Give the location of every parasitized red blood cell.
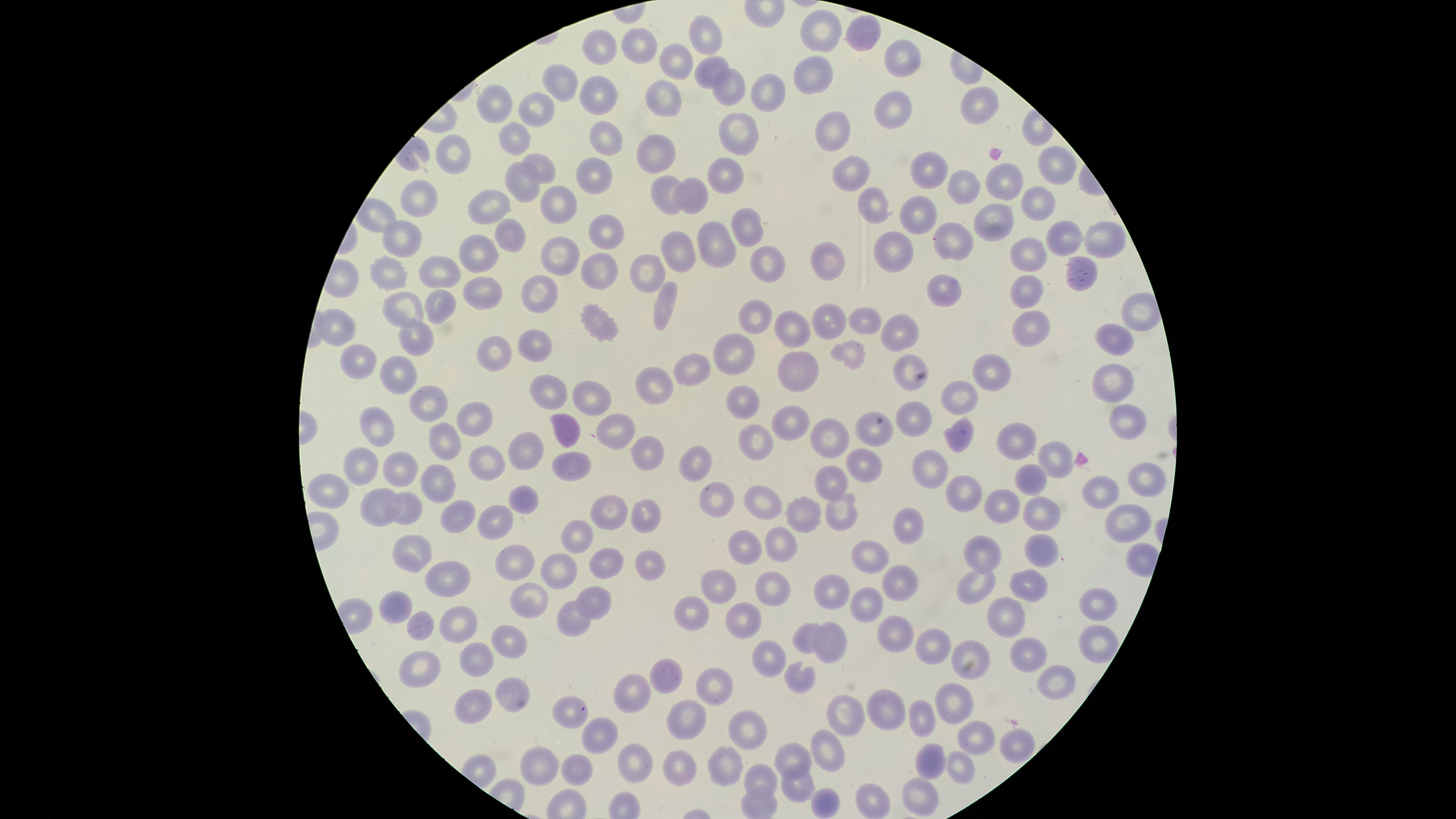
No parasitized red blood cells identified.

uninfected_red_blood_cells: 'approximate marker points, in pixels from the top-left corner: (x=822, y=29), (x=866, y=34), (x=705, y=36), (x=641, y=43), (x=598, y=47), (x=903, y=56), (x=676, y=57), (x=814, y=70), (x=708, y=71), (x=566, y=81), (x=726, y=86), (x=666, y=90), (x=597, y=92), (x=759, y=93), (x=495, y=101), (x=974, y=104), (x=892, y=109), (x=532, y=111), (x=834, y=126), (x=738, y=132), (x=517, y=136), (x=601, y=138), (x=656, y=148), (x=454, y=154), (x=1050, y=162), (x=925, y=163), (x=540, y=167), (x=727, y=170), (x=846, y=172), (x=1005, y=172), (x=594, y=177), (x=962, y=182), (x=520, y=183), (x=669, y=191), (x=701, y=195), (x=1029, y=199), (x=421, y=201), (x=488, y=204), (x=564, y=204), (x=914, y=208), (x=871, y=211), (x=992, y=218), (x=734, y=224), (x=600, y=230), (x=505, y=234), (x=1097, y=236), (x=1067, y=237), (x=398, y=238), (x=668, y=239), (x=706, y=239), (x=957, y=239), (x=886, y=245), (x=472, y=251), (x=1025, y=253), (x=554, y=256), (x=823, y=261), (x=601, y=271), (x=765, y=271), (x=437, y=272), (x=656, y=272), (x=1076, y=272), (x=394, y=274), (x=949, y=287), (x=474, y=293), (x=1021, y=293), (x=539, y=294), (x=663, y=297), (x=405, y=307), (x=437, y=307), (x=863, y=312), (x=755, y=318), (x=591, y=319), (x=827, y=319), (x=794, y=323), (x=1026, y=325), (x=901, y=326), (x=343, y=328), (x=410, y=338), (x=1111, y=341), (x=535, y=343), (x=501, y=351), (x=848, y=351), (x=727, y=352), (x=360, y=360), (x=909, y=363), (x=793, y=365), (x=991, y=366), (x=692, y=368), (x=395, y=372), (x=1115, y=375), (x=658, y=377), (x=551, y=391), (x=960, y=393), (x=592, y=398), (x=742, y=400), (x=423, y=403), (x=913, y=418), (x=470, y=419), (x=790, y=420), (x=1118, y=420), (x=372, y=423), (x=864, y=427), (x=613, y=428), (x=952, y=430), (x=563, y=432), (x=1014, y=436), (x=827, y=437), (x=436, y=440), (x=756, y=441), (x=531, y=449), (x=642, y=451), (x=699, y=454), (x=1055, y=455), (x=862, y=463), (x=574, y=465), (x=477, y=466), (x=931, y=466), (x=358, y=467), (x=402, y=467), (x=1025, y=474), (x=1140, y=481), (x=829, y=482), (x=437, y=484), (x=326, y=487), (x=963, y=489), (x=517, y=494), (x=719, y=495), (x=1095, y=496), (x=760, y=498), (x=380, y=502), (x=409, y=502), (x=996, y=505), (x=603, y=510), (x=643, y=510), (x=834, y=511), (x=457, y=512), (x=491, y=516), (x=801, y=516), (x=912, y=519), (x=1037, y=520), (x=1117, y=521), (x=577, y=531), (x=742, y=538), (x=778, y=539), (x=990, y=546), (x=405, y=547), (x=1038, y=549), (x=606, y=550), (x=871, y=555), (x=638, y=556), (x=508, y=561), (x=555, y=567), (x=447, y=577), (x=712, y=580), (x=974, y=581), (x=1031, y=583), (x=897, y=584), (x=771, y=588), (x=833, y=591), (x=595, y=596), (x=532, y=598), (x=866, y=601), (x=398, y=604), (x=1099, y=606), (x=693, y=612), (x=742, y=613), (x=565, y=614), (x=459, y=619), (x=1004, y=619), (x=423, y=621), (x=803, y=630), (x=889, y=633), (x=505, y=637), (x=833, y=638), (x=1096, y=638), (x=932, y=645), (x=1021, y=653), (x=474, y=659), (x=769, y=660), (x=967, y=660), (x=418, y=665), (x=796, y=672), (x=669, y=675), (x=1045, y=678), (x=711, y=679), (x=506, y=693), (x=632, y=694), (x=956, y=704), (x=473, y=705), (x=886, y=705), (x=920, y=712), (x=847, y=713), (x=563, y=715), (x=681, y=721), (x=743, y=723), (x=972, y=730), (x=602, y=734), (x=1016, y=742), (x=828, y=747), (x=788, y=757), (x=630, y=759), (x=928, y=759), (x=726, y=760), (x=958, y=765), (x=542, y=767), (x=576, y=767), (x=679, y=769), (x=758, y=781), (x=796, y=789), (x=915, y=793), (x=825, y=802)'
stain: Giemsa
field_of_view: single
visible_region: circular
image_size: 1456×819 pixels
preparation: thin smear of blood
capture: smartphone photograph through the microscope eyepiece